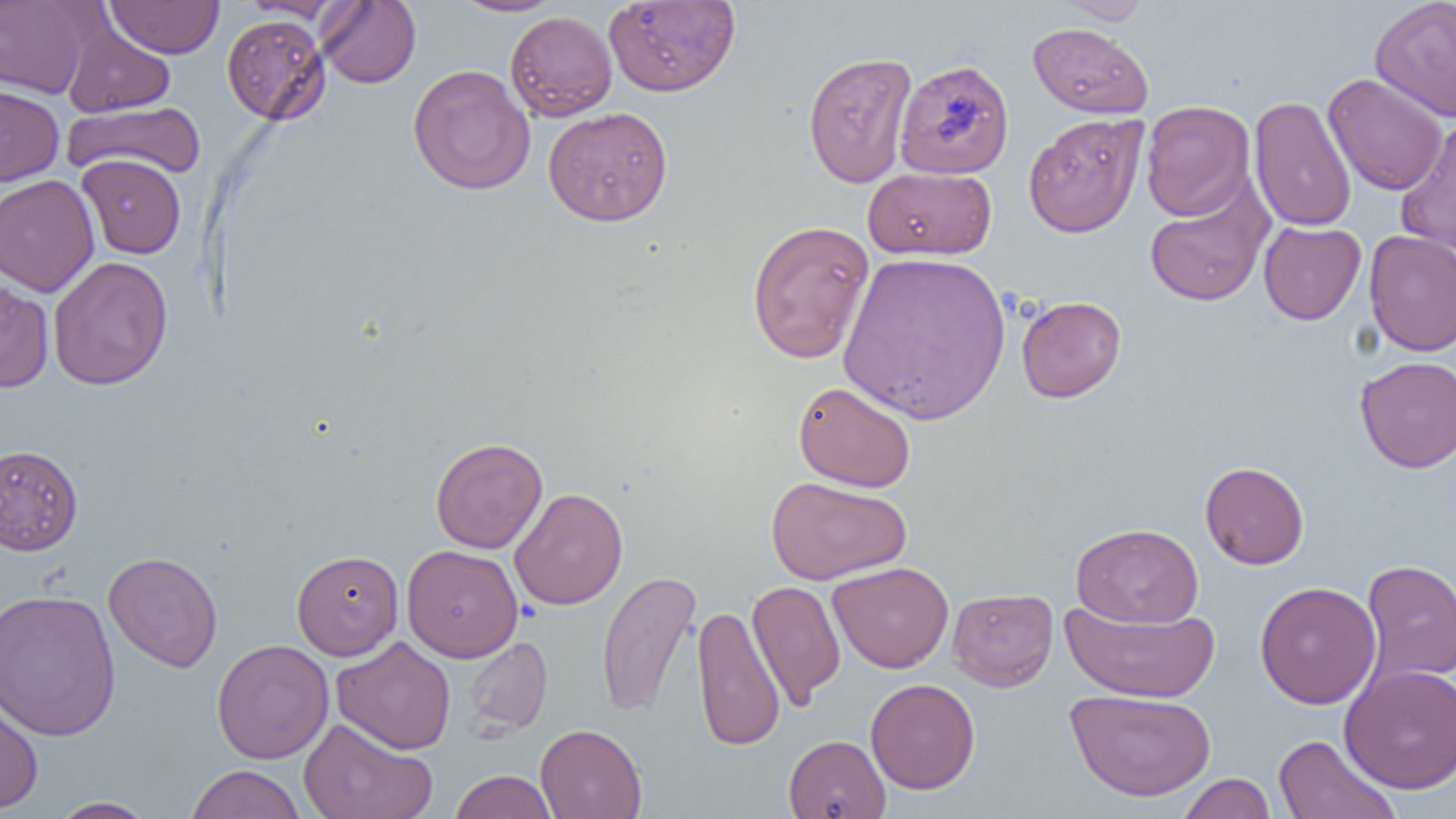
{
  "slide_level_diagnosis": "no evidence of blood parasites",
  "modality": "optical microscopy",
  "preparation": "thin blood film",
  "image_size": "1456×819 pixels",
  "uninfected_red_blood_cell_locations": "approximate bounding boxes as (x1,y1)-(x2,y2) corner pairs in pixels: (316,0)-(421,89), (451,0)-(565,16), (604,0)-(740,97), (1055,0)-(1153,24), (1369,0)-(1456,122), (0,1)-(94,98), (106,1)-(224,59), (239,1)-(348,21), (505,10)-(617,121), (222,14)-(331,126), (61,22)-(175,117), (1027,22)-(1153,118), (803,51)-(918,188), (893,58)-(1015,179), (408,64)-(536,195), (1323,73)-(1449,196), (0,84)-(64,186), (1249,96)-(1357,232), (1140,100)-(1255,221), (62,101)-(206,180), (543,106)-(673,226), (1023,113)-(1148,237), (1395,120)-(1456,256), (77,154)-(186,259), (863,166)-(996,260), (0,174)-(99,298), (1145,179)-(1273,307), (746,220)-(875,364), (1258,221)-(1366,325), (1363,230)-(1456,357), (838,251)-(1011,424), (47,256)-(173,391), (0,275)-(54,393), (1016,295)-(1126,403), (1354,355)-(1456,472), (793,381)-(916,493), (430,437)-(547,553), (0,444)-(83,556), (1200,461)-(1309,569), (766,475)-(912,585), (510,487)-(628,609), (1071,523)-(1204,628), (402,544)-(523,662), (291,549)-(403,660), (103,551)-(223,672), (1360,558)-(1456,685), (828,561)-(954,673), (596,569)-(701,718), (747,580)-(845,709), (1254,581)-(1382,709), (947,587)-(1058,692), (0,588)-(121,742), (1060,597)-(1220,705), (692,603)-(785,752), (331,636)-(456,754), (463,636)-(553,736), (212,639)-(334,763), (1340,664)-(1456,794), (865,678)-(980,794), (0,688)-(44,814), (1065,688)-(1216,801), (298,718)-(437,819), (535,723)-(647,819), (783,734)-(890,818), (1273,734)-(1401,819), (184,764)-(306,819), (449,770)-(557,819), (1176,773)-(1276,818), (49,797)-(157,818)",
  "field_of_view": "one of a larger specimen",
  "magnification": "1000x"
}